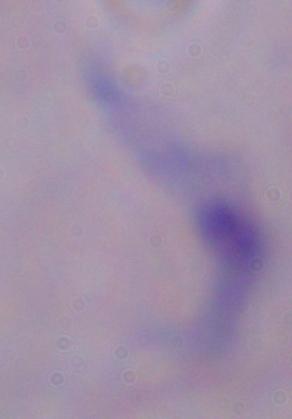
Summary:
  - Modality: photomicrograph
  - Magnification: 1000x
  - Identification: trypanosome